Give the extent of all uninfected red blood cells.
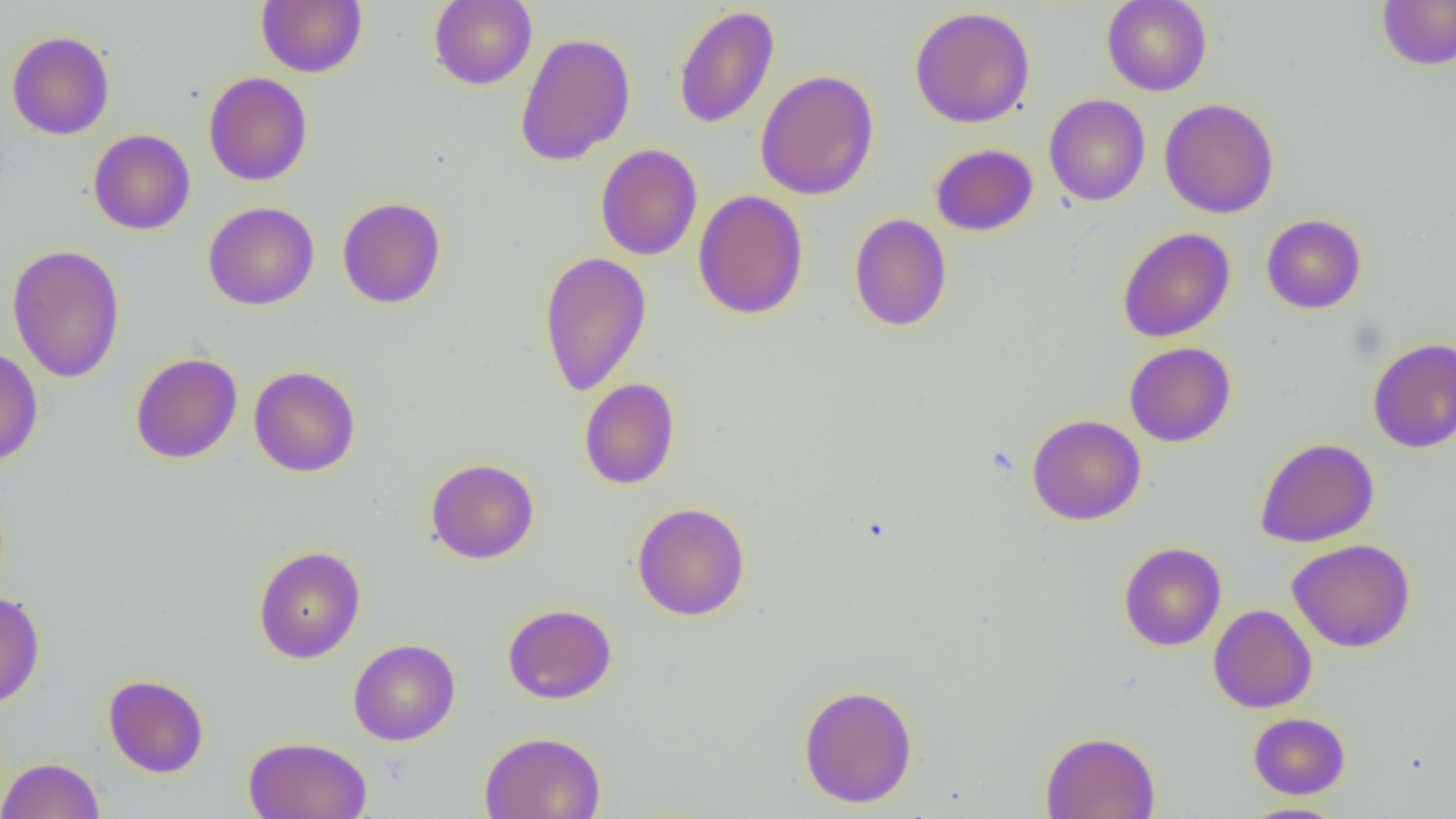

Approximate bounding boxes as (x1, y1, x2, y2) in pixels.
Uninfected red blood cells: (256, 0, 367, 77), (428, 0, 537, 89), (1101, 0, 1212, 96), (1376, 0, 1456, 71), (673, 5, 779, 130), (909, 6, 1036, 128), (6, 30, 115, 140), (514, 32, 636, 166), (755, 69, 879, 200), (203, 72, 313, 186), (1043, 94, 1150, 206), (1158, 98, 1279, 218), (88, 129, 195, 235), (595, 143, 702, 261), (930, 143, 1038, 236), (693, 190, 809, 320), (336, 196, 447, 309), (203, 202, 319, 310), (849, 214, 952, 332), (1261, 214, 1367, 314), (1117, 227, 1235, 342), (7, 244, 126, 383), (538, 250, 652, 397), (1367, 338, 1456, 453), (1124, 342, 1236, 447), (0, 347, 43, 466), (130, 353, 242, 464), (248, 365, 361, 478), (579, 377, 680, 490), (1027, 414, 1146, 525), (1255, 438, 1380, 547), (425, 458, 539, 564), (631, 502, 750, 621), (1287, 539, 1416, 652), (1119, 542, 1227, 650), (253, 545, 366, 663), (0, 591, 45, 709), (502, 603, 617, 704), (1209, 604, 1317, 713), (348, 638, 461, 746), (103, 673, 209, 778), (799, 684, 918, 809), (1248, 712, 1350, 799), (1040, 730, 1161, 819), (479, 731, 606, 819), (243, 736, 373, 819), (0, 757, 105, 819), (1238, 803, 1349, 819).

Summary:
  - Slide-level diagnosis: no evidence of blood parasites
  - Preparation: thin blood film
  - Magnification: 1000x
  - Image size: 1456×819 pixels
  - Modality: light microscopy
  - Field of view: one of a larger specimen